Identify the parasite.
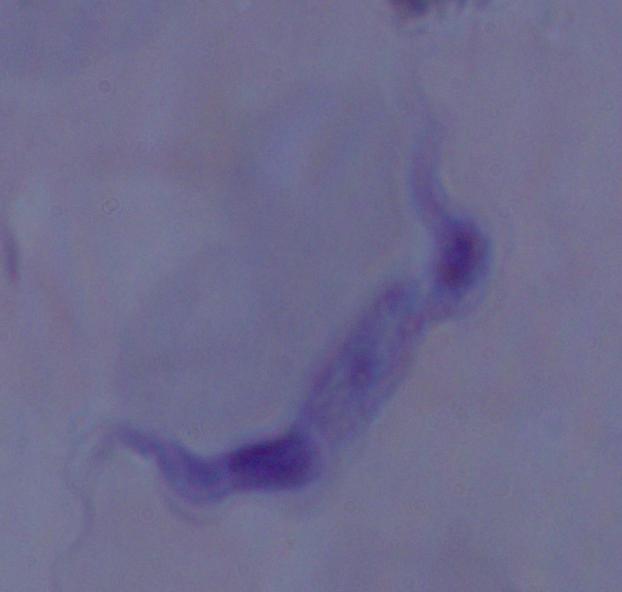

A trypanosome.

Summary:
  - Magnification: 1000x
  - Modality: photomicrograph